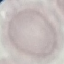

malaria status = uninfected
preparation = thin blood film
capture = smartphone through the microscope eyepiece
image type = cell patch, automatically extracted from a larger field of view and resized to 64 × 64 pixels
stain = Giemsa